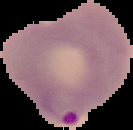
preparation = thin blood film
image type = segmented cell region on a black background
malaria status = parasitized
image size = 133×130 pixels